Give the preparation type.
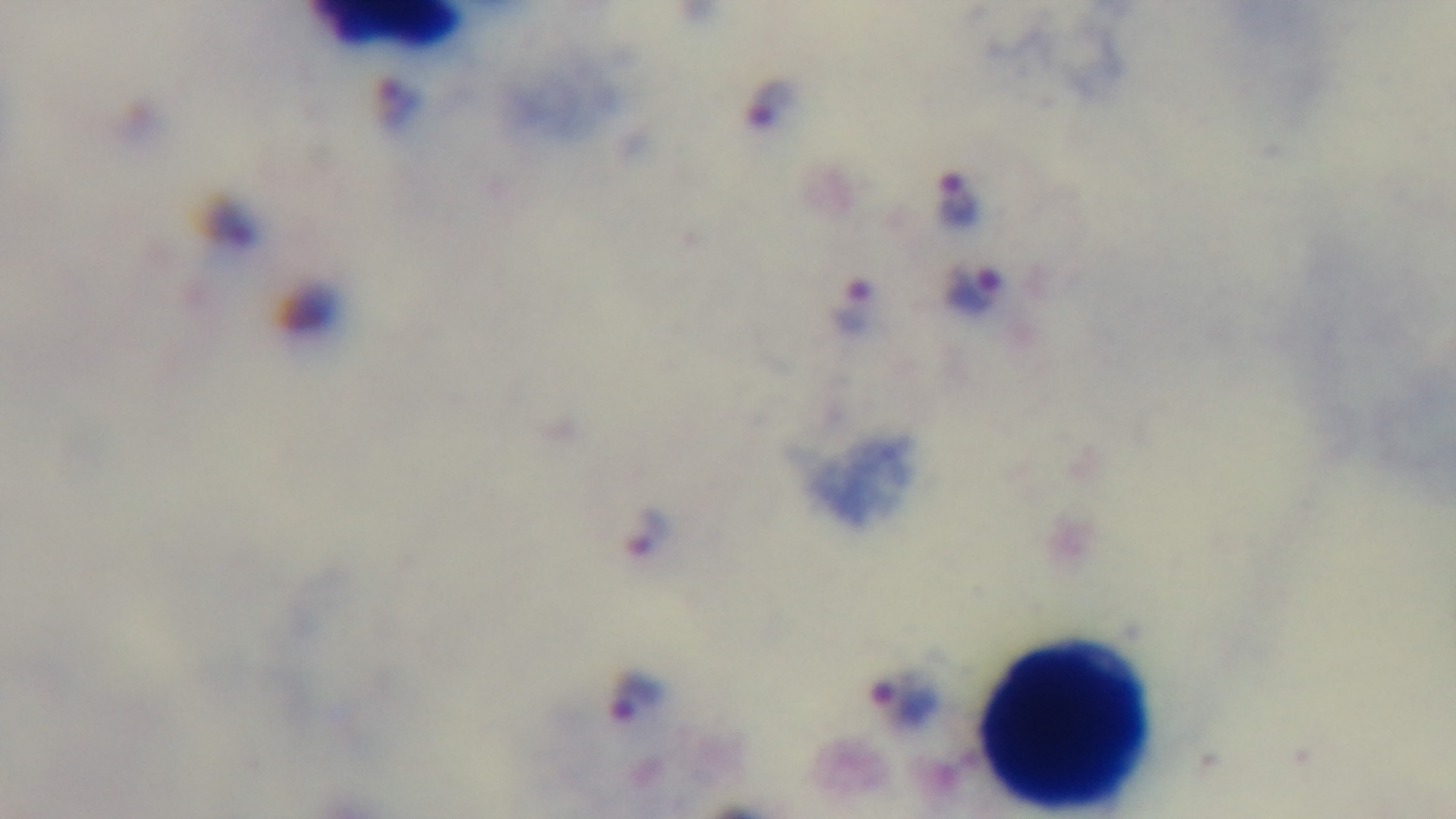
It is a thick blood film.

objective: 100x oil immersion
field_of_view: one from the slide
malaria_status: infected
capture: mounted 4K digital camera
modality: light microscopy
stain: Giemsa